State which cell type is depicted.
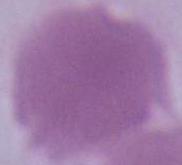
This is an erythrocyte.

magnification = 1000x
modality = micrograph